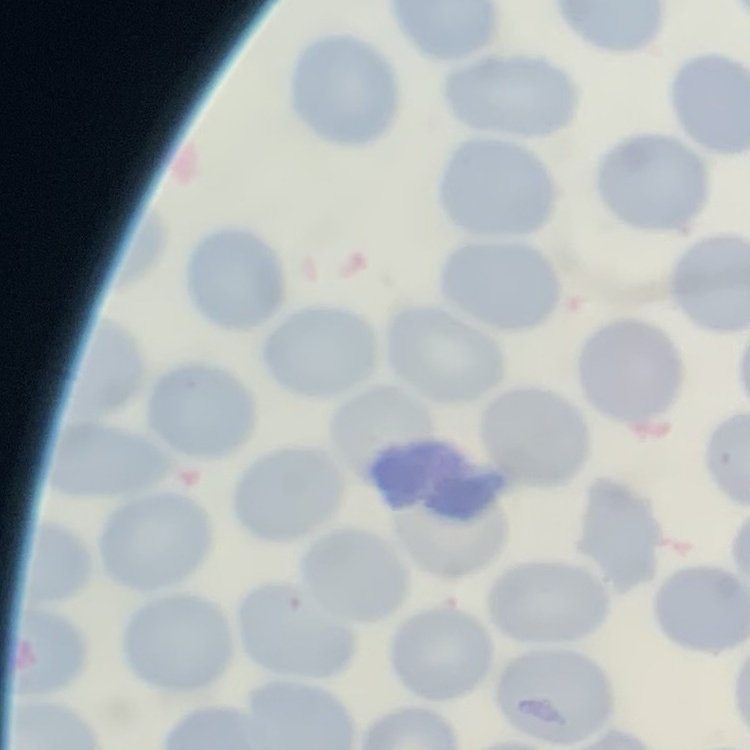
erythrocyte_morphology: no rouleaux formation
stain: Field's or Giemsa
preparation: thin blood film
image_type: square crop of a larger photomicrograph